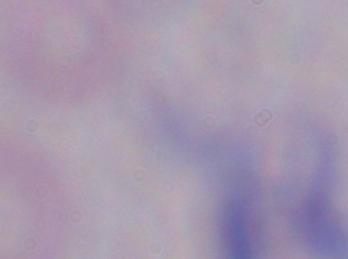
Summary:
  - Magnification: 1000x
  - Modality: photomicrograph
  - Identification: trypanosome